Locate every blood parasite and identify its species.
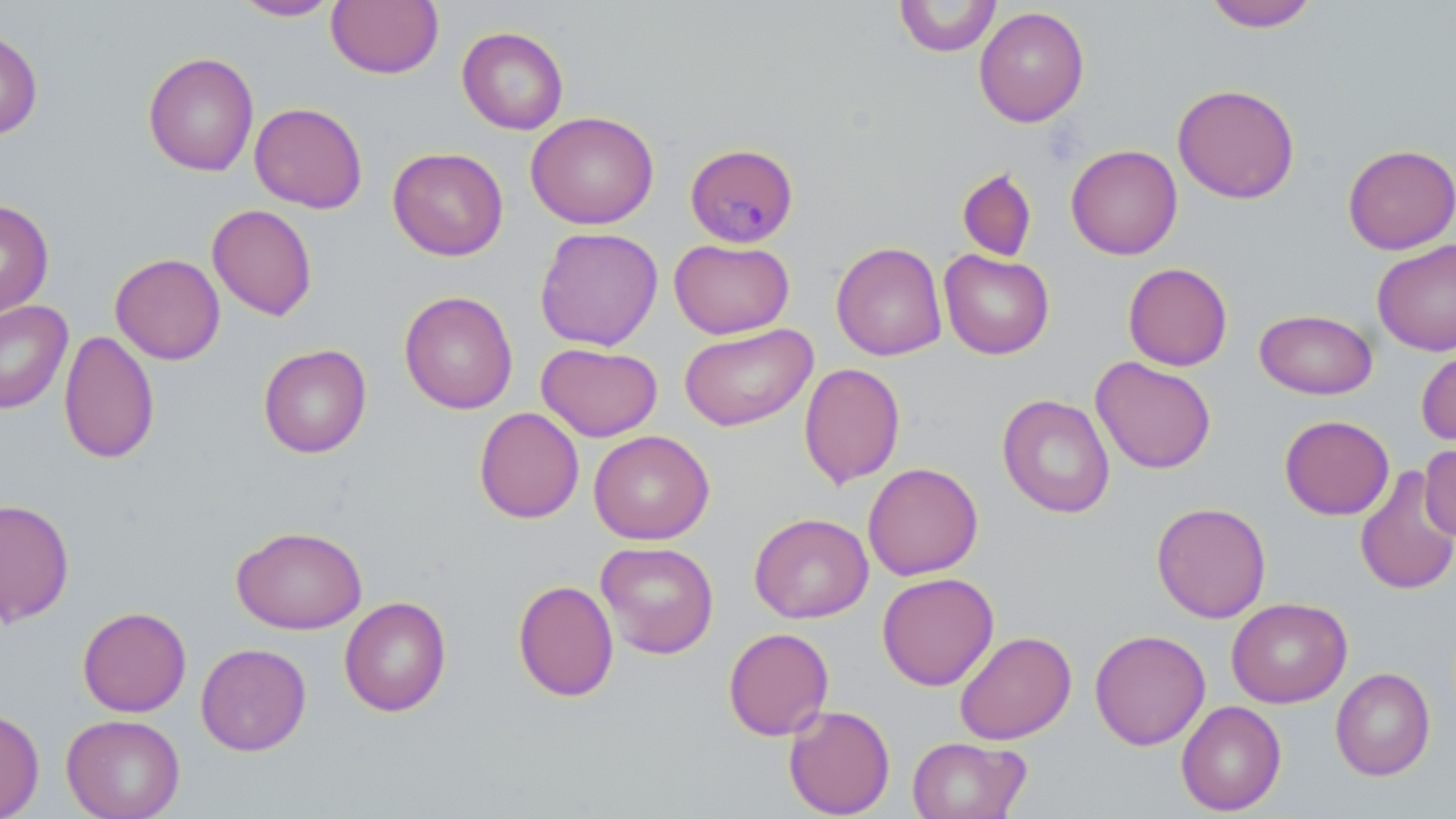
Approximate bounding boxes as named x1/y1/x2/y2 corners in pixels.
Plasmodium malariae-infected red blood cells: (x1=684, y1=142, x2=799, y2=248).
No Plasmodium falciparum, Plasmodium ovale, Plasmodium vivax, Babesia divergens, or Trypanosoma brucei observed.

Summary:
  - Uninfected red blood cell locations: (x1=232, y1=0, x2=340, y2=21), (x1=326, y1=0, x2=444, y2=79), (x1=894, y1=0, x2=1001, y2=57), (x1=1202, y1=0, x2=1320, y2=31), (x1=973, y1=6, x2=1090, y2=127), (x1=457, y1=26, x2=569, y2=134), (x1=0, y1=29, x2=43, y2=141), (x1=142, y1=51, x2=259, y2=177), (x1=1172, y1=83, x2=1300, y2=204), (x1=249, y1=102, x2=367, y2=213), (x1=525, y1=111, x2=659, y2=229), (x1=1342, y1=143, x2=1456, y2=255), (x1=1065, y1=144, x2=1183, y2=260), (x1=388, y1=147, x2=509, y2=261), (x1=957, y1=168, x2=1037, y2=262), (x1=0, y1=198, x2=54, y2=318), (x1=207, y1=204, x2=318, y2=321), (x1=534, y1=226, x2=663, y2=351), (x1=669, y1=238, x2=794, y2=339), (x1=1371, y1=239, x2=1456, y2=356), (x1=831, y1=241, x2=947, y2=361), (x1=939, y1=249, x2=1055, y2=359), (x1=110, y1=253, x2=226, y2=365), (x1=1123, y1=262, x2=1233, y2=371), (x1=399, y1=290, x2=518, y2=414), (x1=0, y1=300, x2=73, y2=414), (x1=1254, y1=308, x2=1378, y2=399), (x1=679, y1=323, x2=818, y2=432), (x1=58, y1=330, x2=160, y2=464), (x1=536, y1=342, x2=663, y2=442), (x1=258, y1=343, x2=372, y2=458), (x1=1416, y1=346, x2=1456, y2=446), (x1=1091, y1=356, x2=1216, y2=474), (x1=799, y1=362, x2=905, y2=489), (x1=997, y1=394, x2=1115, y2=519), (x1=474, y1=407, x2=584, y2=524), (x1=1279, y1=415, x2=1394, y2=520), (x1=588, y1=430, x2=715, y2=545), (x1=1419, y1=442, x2=1456, y2=543), (x1=863, y1=462, x2=983, y2=580), (x1=1354, y1=465, x2=1456, y2=597), (x1=0, y1=498, x2=75, y2=626), (x1=1151, y1=502, x2=1272, y2=623), (x1=749, y1=513, x2=874, y2=624), (x1=231, y1=525, x2=367, y2=634), (x1=595, y1=540, x2=719, y2=659), (x1=877, y1=572, x2=999, y2=691), (x1=512, y1=579, x2=619, y2=702), (x1=339, y1=596, x2=451, y2=717), (x1=1226, y1=597, x2=1352, y2=707), (x1=78, y1=606, x2=191, y2=717), (x1=723, y1=627, x2=834, y2=741), (x1=1089, y1=629, x2=1211, y2=750), (x1=954, y1=630, x2=1076, y2=745), (x1=195, y1=642, x2=311, y2=756), (x1=1330, y1=667, x2=1436, y2=781), (x1=1176, y1=700, x2=1286, y2=816), (x1=783, y1=704, x2=895, y2=818), (x1=0, y1=708, x2=45, y2=819), (x1=61, y1=714, x2=185, y2=819), (x1=907, y1=736, x2=1031, y2=819)
  - Slide-level diagnosis: Plasmodium malariae
  - Magnification: 1000x
  - Stain: May-Grünwald-Giemsa
  - Preparation: thin blood smear
  - Field of view: single
  - Image size: 1456×819 pixels
  - Modality: optical microscopy